Identify the parasite.
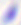

This is Toxoplasma gondii.

{
  "modality": "photomicrograph",
  "magnification": "400x"
}